Assess this cell for malaria.
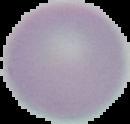
It is uninfected.

Summary:
  - Image type: segmented cell region with the area outside set to black
  - Image size: 130×124 pixels
  - Preparation: thin blood smear